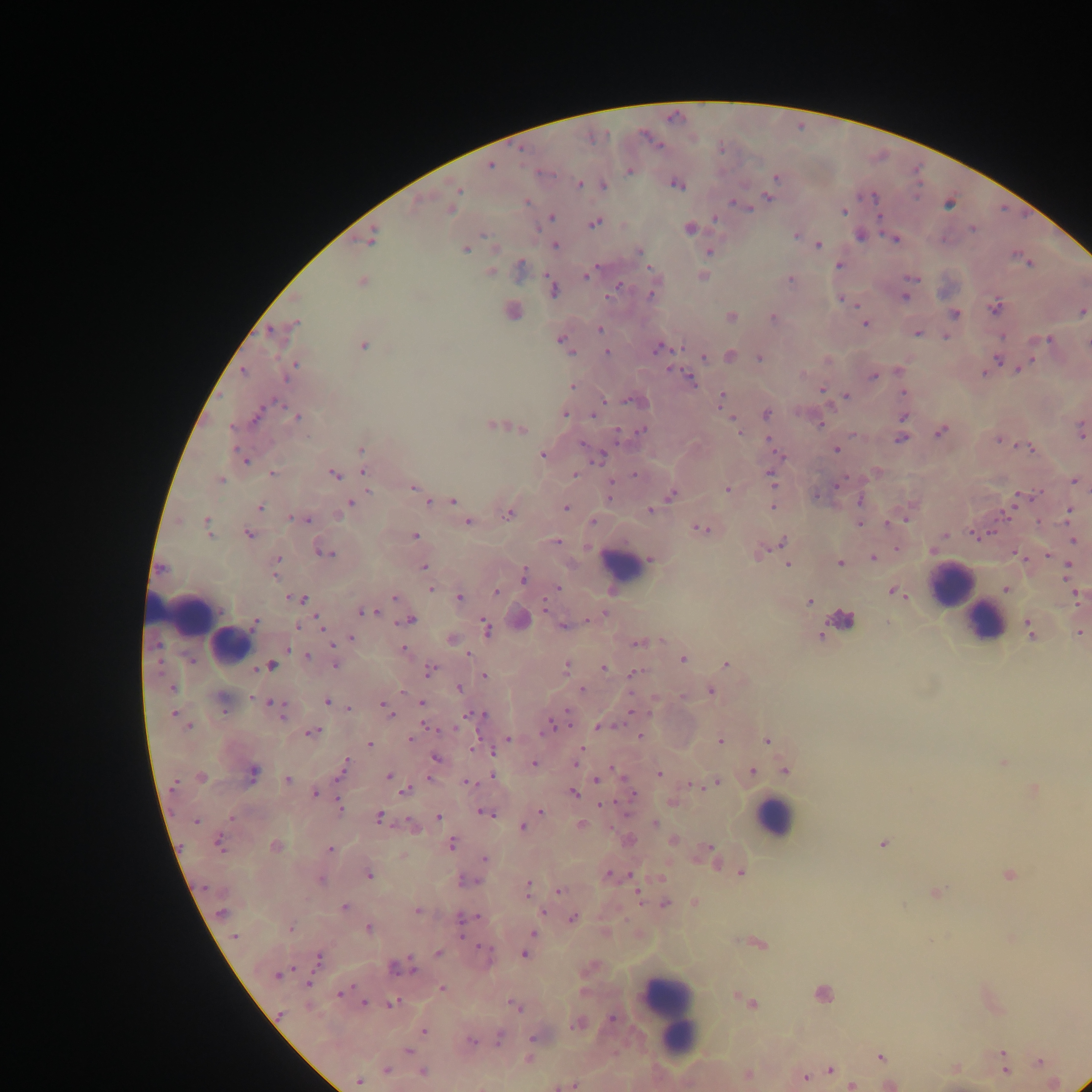

Approximate centers as (x, y) in pixels. Leukocyte locations: (621, 565), (952, 585), (185, 616), (840, 621), (984, 621), (230, 647), (774, 818), (668, 1012). Malaria parasite locations: (490, 165), (629, 171), (775, 177), (579, 183), (676, 183), (603, 185), (457, 189), (454, 197), (768, 197), (418, 201), (527, 201), (734, 203), (742, 205), (747, 207), (451, 209), (843, 211), (550, 217), (715, 218), (594, 221), (689, 228), (972, 228), (796, 235), (860, 235), (371, 236), (895, 238), (555, 245), (818, 245), (465, 248), (495, 249), (638, 251), (708, 251), (1028, 264), (838, 265), (519, 269), (490, 271), (587, 274), (703, 276), (911, 278), (790, 279), (361, 281), (619, 285), (553, 289), (904, 296), (841, 299), (995, 306), (512, 310), (1082, 311), (954, 313), (731, 316), (774, 318), (864, 323), (289, 328), (599, 329), (279, 331), (917, 333), (945, 335), (1045, 339), (562, 341), (363, 344), (659, 348), (607, 351), (716, 355), (729, 356), (759, 356), (704, 357), (998, 360), (293, 367), (1019, 368), (984, 372), (802, 375), (873, 375), (689, 380), (572, 386), (821, 390), (904, 392), (846, 396), (721, 399), (636, 401), (765, 413), (565, 414), (296, 416), (903, 416), (733, 421), (493, 424), (819, 424), (522, 429), (738, 429), (1081, 430), (641, 431), (940, 431), (901, 438), (999, 438), (769, 440), (1025, 446), (361, 449), (836, 449), (779, 454), (544, 455), (598, 455), (244, 459), (364, 471), (271, 473), (333, 474), (574, 474), (771, 477), (220, 480), (1074, 480), (837, 485), (413, 487), (727, 490), (418, 491), (671, 494), (610, 495), (816, 495), (1019, 495), (451, 500), (860, 500), (429, 501), (350, 503), (773, 506), (259, 507), (566, 507), (650, 509), (1069, 510), (1006, 511), (508, 513), (304, 519), (592, 521), (466, 522), (859, 523), (207, 524), (887, 524), (701, 527), (247, 533), (975, 534), (414, 535), (944, 535), (1073, 540), (556, 541), (780, 543), (897, 548), (761, 549), (932, 549), (323, 552), (1048, 553), (1018, 555), (872, 557), (652, 558), (277, 561), (840, 562), (788, 564), (423, 567), (1068, 567), (523, 576), (1006, 588), (431, 589), (557, 589), (497, 592), (894, 592), (1076, 595), (395, 597), (459, 598), (296, 599), (809, 601), (367, 612), (408, 619), (519, 619), (587, 620), (319, 621), (253, 623), (563, 626), (485, 628), (1030, 630), (1079, 632), (819, 634), (350, 638), (451, 639), (638, 642), (403, 650), (467, 653), (306, 656), (682, 658), (335, 663), (725, 663), (270, 665), (566, 666), (604, 668), (429, 670), (633, 674), (484, 676), (172, 687), (459, 688), (582, 689), (710, 690), (327, 701), (222, 702), (421, 703), (347, 707), (278, 709), (386, 709), (632, 712), (473, 714), (176, 715), (564, 718), (554, 722), (600, 726), (548, 727), (311, 732), (639, 736), (410, 739), (719, 739), (767, 740), (506, 741), (369, 744), (435, 757), (578, 759), (1003, 762), (533, 763), (343, 767), (611, 768), (785, 770), (751, 771), (658, 773), (253, 774), (493, 775), (389, 776), (201, 778), (597, 779), (288, 780), (468, 782), (715, 782), (707, 783), (690, 784), (1033, 789), (406, 790), (572, 792), (316, 793), (632, 795), (672, 802), (603, 804), (340, 805), (540, 811), (485, 812), (378, 817), (438, 817), (196, 821), (413, 824), (580, 824), (655, 824), (522, 827), (629, 840), (673, 840), (218, 842), (451, 843), (883, 843), (275, 846), (329, 849), (710, 855), (484, 858), (741, 872), (368, 874), (1007, 874), (607, 875), (632, 876), (321, 879), (468, 879), (526, 888), (559, 891), (935, 892), (665, 903), (694, 903), (343, 907), (417, 911), (543, 911), (221, 912), (572, 917), (463, 918), (290, 928), (368, 928), (531, 935), (234, 936), (757, 942), (438, 953), (525, 953), (484, 955), (317, 960), (398, 965), (278, 974), (442, 988), (342, 992), (823, 994), (743, 1000), (364, 1003), (391, 1003), (751, 1003), (514, 1005), (279, 1016), (613, 1018), (577, 1023), (424, 1031), (535, 1036), (499, 1038), (470, 1040), (407, 1050), (881, 1055), (528, 1057), (1039, 1061), (1003, 1063), (385, 1069), (830, 1069), (954, 1069), (422, 1072), (747, 1075), (804, 1076), (358, 1081), (1052, 1083), (1083, 1083), (572, 1084), (851, 1084), (889, 1084), (563, 1085). Image is 1092×1092 pixels. Photographed through a microscope with a mobile-phone camera. Single field of view. Collected in Ghana. Thick blood smear.